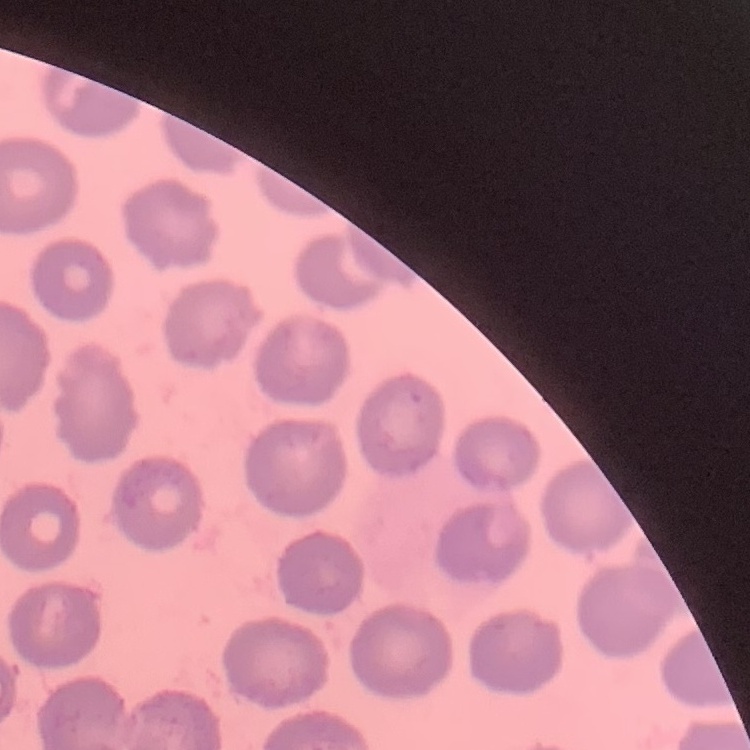 The red blood cells show no rouleaux formation. Square crop of a larger photomicrograph. Field's or Giemsa stain. Thin blood film.